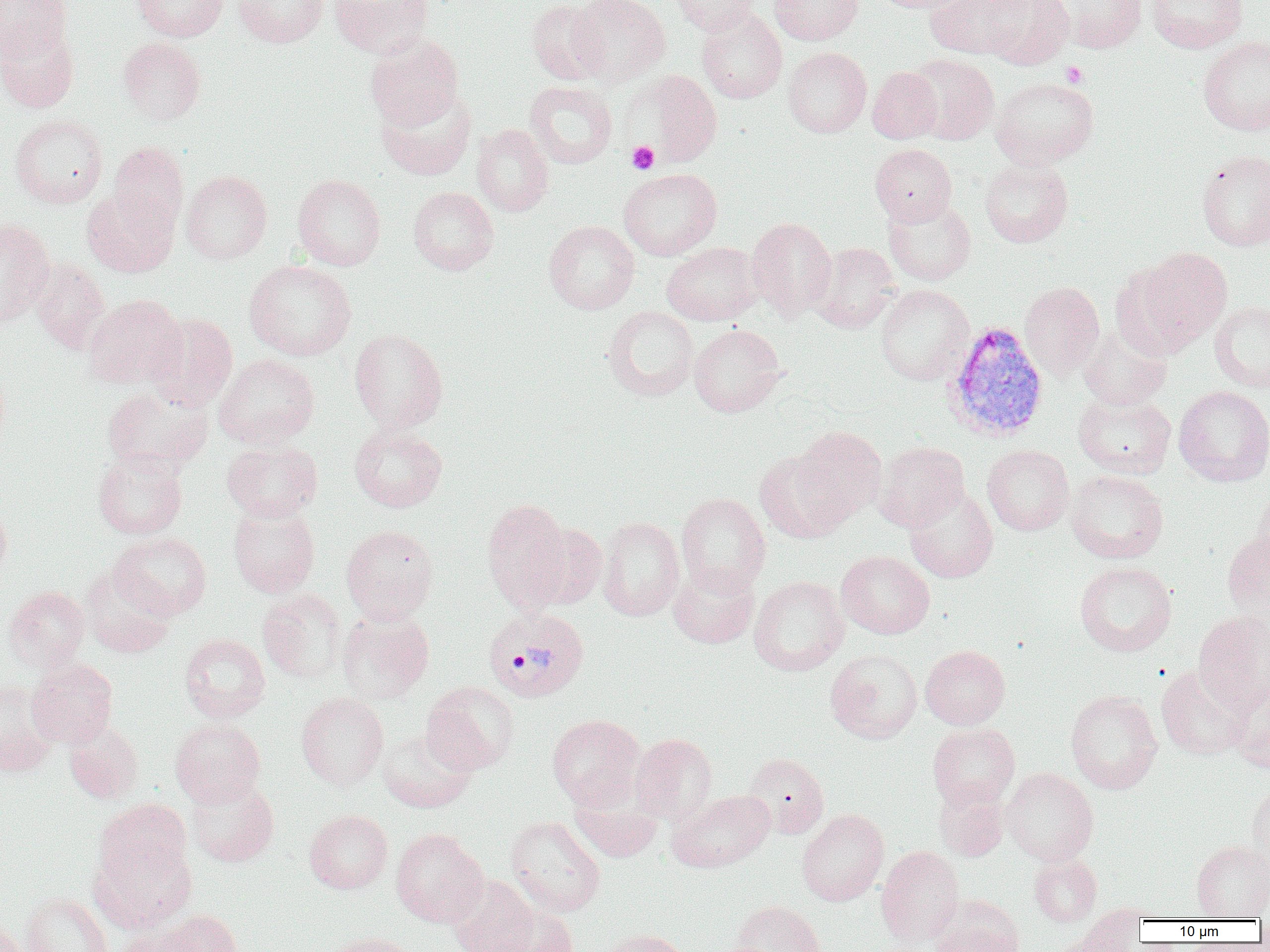

Summary:
  - Coordinate format: approximate bounding boxes as named x1/y1/x2/y2 corners in pixels
  - Plasmodium vivax-infected red blood cell locations: (x1=942, y1=320, x2=1049, y2=443), (x1=483, y1=607, x2=589, y2=702)
  - Uninfected red blood cell locations: (x1=0, y1=0, x2=71, y2=62), (x1=131, y1=0, x2=228, y2=41), (x1=233, y1=0, x2=329, y2=47), (x1=329, y1=0, x2=434, y2=58), (x1=526, y1=0, x2=609, y2=85), (x1=570, y1=0, x2=670, y2=87), (x1=672, y1=0, x2=760, y2=35), (x1=770, y1=0, x2=863, y2=45), (x1=871, y1=0, x2=978, y2=13), (x1=979, y1=0, x2=1074, y2=69), (x1=1146, y1=0, x2=1248, y2=53), (x1=926, y1=1, x2=1028, y2=58), (x1=1052, y1=1, x2=1148, y2=53), (x1=696, y1=7, x2=787, y2=104), (x1=0, y1=20, x2=80, y2=113), (x1=365, y1=33, x2=464, y2=129), (x1=1198, y1=36, x2=1270, y2=135), (x1=118, y1=37, x2=206, y2=125), (x1=783, y1=47, x2=871, y2=138), (x1=905, y1=53, x2=999, y2=145), (x1=867, y1=66, x2=942, y2=144), (x1=632, y1=70, x2=723, y2=167), (x1=991, y1=77, x2=1099, y2=169), (x1=525, y1=81, x2=617, y2=169), (x1=376, y1=86, x2=477, y2=180), (x1=9, y1=114, x2=108, y2=208), (x1=472, y1=123, x2=554, y2=217), (x1=108, y1=141, x2=189, y2=235), (x1=870, y1=144, x2=957, y2=226), (x1=1197, y1=150, x2=1270, y2=250), (x1=979, y1=158, x2=1073, y2=247), (x1=618, y1=168, x2=722, y2=260), (x1=181, y1=170, x2=272, y2=264), (x1=292, y1=174, x2=386, y2=271), (x1=408, y1=186, x2=499, y2=275), (x1=81, y1=187, x2=178, y2=278), (x1=883, y1=197, x2=977, y2=286), (x1=746, y1=217, x2=837, y2=320), (x1=0, y1=218, x2=55, y2=327), (x1=544, y1=220, x2=639, y2=314), (x1=661, y1=242, x2=763, y2=325), (x1=809, y1=242, x2=901, y2=333), (x1=1130, y1=246, x2=1233, y2=350), (x1=30, y1=259, x2=110, y2=354), (x1=244, y1=260, x2=356, y2=360), (x1=1020, y1=281, x2=1104, y2=378), (x1=875, y1=284, x2=973, y2=385), (x1=84, y1=294, x2=186, y2=388), (x1=1209, y1=301, x2=1270, y2=393), (x1=603, y1=306, x2=698, y2=401), (x1=144, y1=313, x2=238, y2=410), (x1=1078, y1=323, x2=1172, y2=410), (x1=689, y1=324, x2=786, y2=417), (x1=349, y1=328, x2=448, y2=433), (x1=213, y1=353, x2=320, y2=448), (x1=102, y1=385, x2=213, y2=473), (x1=1173, y1=385, x2=1270, y2=486), (x1=1073, y1=392, x2=1176, y2=478), (x1=349, y1=423, x2=447, y2=513), (x1=794, y1=427, x2=887, y2=522), (x1=222, y1=439, x2=322, y2=522), (x1=874, y1=441, x2=969, y2=532), (x1=982, y1=445, x2=1074, y2=535), (x1=754, y1=449, x2=853, y2=543), (x1=93, y1=451, x2=187, y2=539), (x1=1066, y1=470, x2=1169, y2=564), (x1=904, y1=485, x2=998, y2=583), (x1=1251, y1=486, x2=1270, y2=575), (x1=676, y1=493, x2=771, y2=595), (x1=482, y1=499, x2=572, y2=611), (x1=0, y1=503, x2=12, y2=584), (x1=228, y1=503, x2=320, y2=597), (x1=597, y1=517, x2=685, y2=621), (x1=523, y1=522, x2=607, y2=610), (x1=341, y1=524, x2=439, y2=623), (x1=1221, y1=530, x2=1270, y2=621), (x1=109, y1=531, x2=212, y2=620), (x1=836, y1=550, x2=935, y2=639), (x1=1074, y1=561, x2=1177, y2=656), (x1=668, y1=562, x2=759, y2=648), (x1=81, y1=565, x2=176, y2=658), (x1=749, y1=575, x2=849, y2=676), (x1=4, y1=586, x2=89, y2=671), (x1=258, y1=589, x2=346, y2=684), (x1=336, y1=609, x2=434, y2=704), (x1=1193, y1=610, x2=1270, y2=714), (x1=179, y1=633, x2=270, y2=723), (x1=920, y1=645, x2=1010, y2=729), (x1=825, y1=649, x2=922, y2=744), (x1=26, y1=659, x2=118, y2=747), (x1=1156, y1=665, x2=1252, y2=760), (x1=1229, y1=679, x2=1270, y2=774), (x1=0, y1=680, x2=56, y2=778), (x1=421, y1=681, x2=519, y2=775), (x1=1065, y1=689, x2=1163, y2=794), (x1=296, y1=692, x2=389, y2=790), (x1=547, y1=714, x2=645, y2=809), (x1=170, y1=717, x2=265, y2=807), (x1=63, y1=720, x2=144, y2=803), (x1=928, y1=723, x2=1020, y2=808), (x1=377, y1=727, x2=476, y2=812), (x1=630, y1=733, x2=717, y2=824), (x1=743, y1=752, x2=829, y2=838), (x1=1003, y1=767, x2=1098, y2=865), (x1=186, y1=776, x2=279, y2=867), (x1=933, y1=780, x2=1010, y2=860), (x1=569, y1=783, x2=663, y2=862), (x1=1247, y1=783, x2=1270, y2=872), (x1=667, y1=789, x2=775, y2=872), (x1=94, y1=799, x2=192, y2=885), (x1=797, y1=808, x2=889, y2=906), (x1=304, y1=809, x2=393, y2=894), (x1=505, y1=816, x2=605, y2=917), (x1=391, y1=828, x2=488, y2=927), (x1=91, y1=834, x2=197, y2=933), (x1=1191, y1=840, x2=1270, y2=919), (x1=876, y1=846, x2=964, y2=947), (x1=1029, y1=854, x2=1102, y2=927), (x1=447, y1=875, x2=539, y2=952), (x1=22, y1=893, x2=112, y2=952), (x1=930, y1=895, x2=1024, y2=952), (x1=731, y1=900, x2=825, y2=952), (x1=492, y1=904, x2=579, y2=952), (x1=160, y1=910, x2=243, y2=952), (x1=0, y1=919, x2=27, y2=952), (x1=115, y1=924, x2=205, y2=952), (x1=598, y1=928, x2=692, y2=952), (x1=324, y1=932, x2=420, y2=952), (x1=1046, y1=933, x2=1133, y2=952)
  - Platelet locations: (x1=1061, y1=61, x2=1088, y2=87), (x1=627, y1=141, x2=659, y2=174)
  - Slide-level diagnosis: Plasmodium vivax
  - Field of view: single
  - Preparation: thin blood film
  - Modality: optical microscopy
  - Magnification: 1000x
  - Image size: 1270×952 pixels